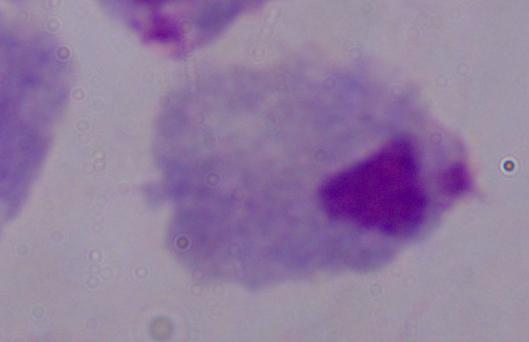
Captured at 1000x magnification. Photomicrograph. A trichomonad is shown.